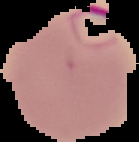
image size = 139×142 pixels
preparation = thin blood smear
image type = segmented cell region on a black background
result = malaria parasites identified